Assess this cell for malaria.
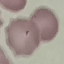

It is uninfected.

image type = automatically extracted cell patch, resized to 64 × 64 pixels
stain = Giemsa
capture = smartphone through the microscope eyepiece
preparation = thin smear